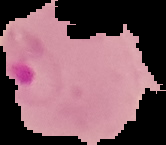
Summary:
  - Preparation: thin blood film
  - Result: malaria parasites detected
  - Image size: 166×145 pixels
  - Image type: cell region segmented out of the field of view; surrounding area masked to black